Outline each blood parasite and name the species.
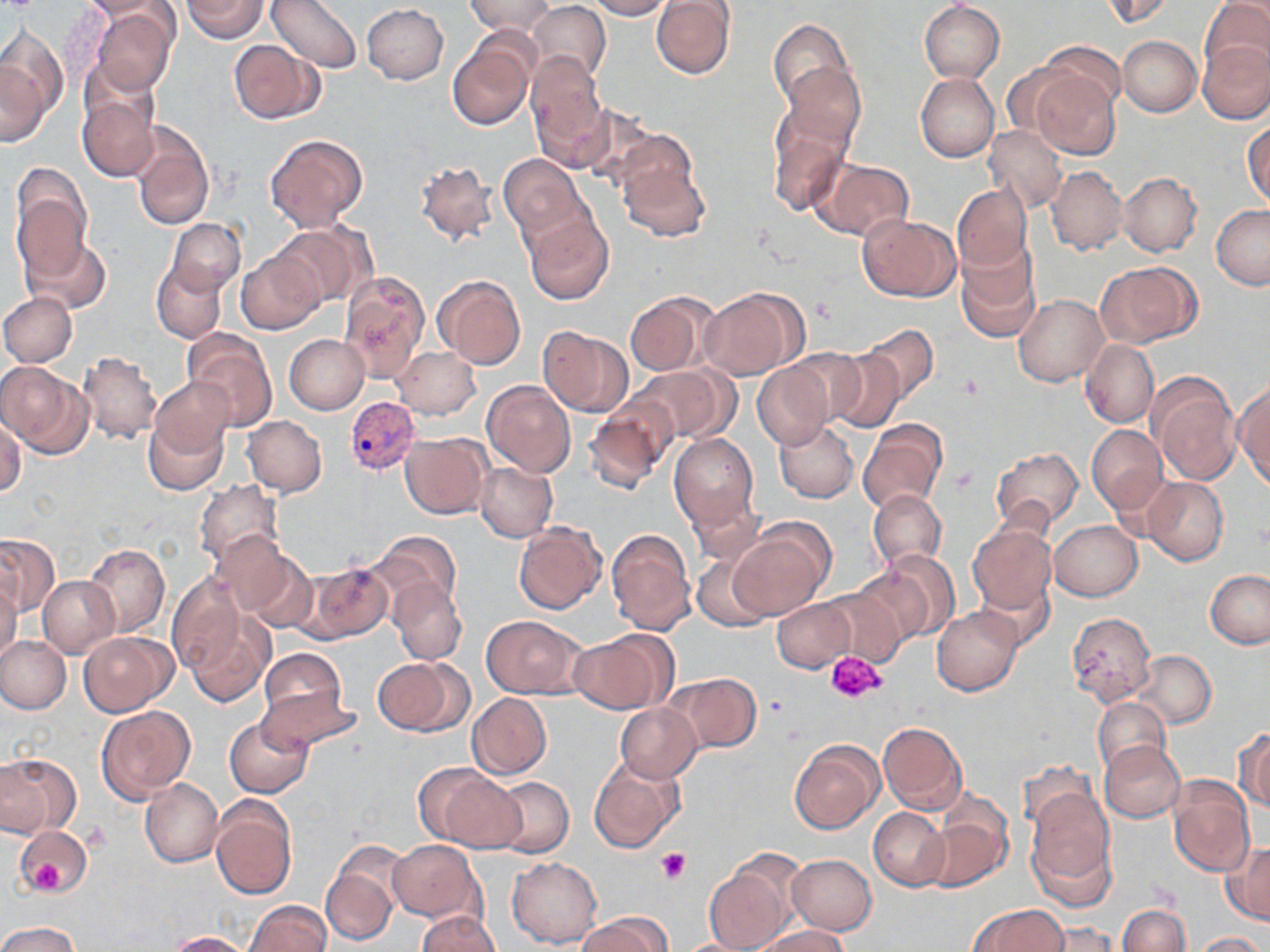
Approximate bounding boxes as (x1, y1, x2, y2) in pixels.
Plasmodium vivax-infected red blood cells: (345, 396, 419, 474).
No Plasmodium falciparum, Plasmodium ovale, Plasmodium malariae, Babesia divergens, or Trypanosoma brucei observed.

slide-level diagnosis = Plasmodium vivax
uninfected red blood cell locations = approximate bounding boxes as (x1, y1, x2, y2) in pixels: (81, 0, 168, 20), (181, 0, 269, 41), (267, 0, 361, 73), (466, 0, 552, 37), (585, 0, 671, 19), (651, 0, 735, 79), (1099, 0, 1174, 26), (1201, 0, 1270, 78), (919, 1, 1005, 82), (527, 2, 611, 84), (361, 4, 448, 84), (90, 6, 177, 95), (769, 19, 852, 109), (0, 25, 70, 124), (1118, 35, 1203, 117), (229, 39, 322, 123), (447, 39, 534, 130), (1199, 40, 1270, 124), (1036, 41, 1125, 123), (526, 53, 609, 165), (1, 56, 51, 146), (782, 63, 866, 149), (1031, 70, 1121, 160), (915, 74, 999, 162), (76, 91, 159, 183), (577, 104, 661, 190), (768, 108, 852, 216), (130, 121, 215, 230), (1243, 121, 1269, 209), (984, 125, 1067, 212), (264, 134, 367, 232), (499, 154, 585, 243), (616, 158, 710, 243), (414, 159, 500, 247), (812, 159, 914, 242), (1045, 166, 1126, 255), (1118, 172, 1202, 257), (952, 183, 1033, 274), (11, 186, 91, 282), (1211, 204, 1270, 289), (523, 212, 613, 305), (858, 214, 959, 301), (166, 218, 245, 295), (272, 222, 372, 307), (24, 235, 111, 315), (958, 243, 1042, 342), (235, 251, 326, 335), (152, 261, 226, 343), (1097, 262, 1200, 348), (338, 271, 429, 383), (435, 275, 526, 370), (701, 289, 803, 380), (0, 292, 76, 366), (626, 292, 713, 377), (1014, 294, 1107, 387), (858, 324, 939, 403), (538, 326, 632, 417), (184, 331, 278, 430), (284, 334, 369, 414), (1081, 339, 1159, 429), (392, 347, 481, 419), (783, 347, 869, 427), (826, 350, 905, 433), (75, 351, 162, 445), (752, 362, 834, 450), (0, 363, 89, 456), (629, 365, 735, 446), (1148, 373, 1241, 485), (151, 376, 234, 460), (1233, 378, 1270, 489), (482, 379, 575, 477), (584, 400, 674, 492), (143, 410, 229, 496), (0, 415, 25, 497), (243, 416, 327, 496), (857, 419, 948, 515), (773, 420, 859, 503), (1086, 425, 1166, 513), (401, 433, 490, 519), (669, 433, 760, 530), (991, 447, 1082, 531), (474, 463, 558, 542), (1142, 477, 1229, 565), (194, 480, 283, 567), (868, 489, 946, 572), (685, 494, 765, 568), (514, 520, 607, 614), (1049, 520, 1142, 600), (729, 522, 832, 619), (967, 524, 1056, 614), (606, 528, 696, 635), (373, 531, 461, 612), (209, 532, 292, 613), (0, 533, 57, 617), (84, 542, 169, 638), (870, 549, 960, 643), (238, 551, 316, 634), (692, 553, 773, 631), (301, 562, 393, 643), (1206, 569, 1270, 650), (165, 575, 244, 677), (974, 575, 1057, 652), (39, 576, 120, 657), (0, 577, 20, 664), (391, 580, 467, 665), (818, 584, 910, 666), (771, 598, 855, 672), (931, 606, 1024, 696), (182, 610, 274, 706), (1066, 612, 1156, 707), (481, 614, 588, 699), (571, 629, 677, 714), (79, 632, 176, 717), (0, 635, 72, 714), (257, 648, 350, 732), (1134, 649, 1216, 728), (372, 657, 468, 737), (668, 672, 761, 754), (256, 684, 362, 752), (467, 692, 553, 780), (1092, 696, 1171, 776), (614, 704, 702, 783), (97, 706, 195, 804), (225, 717, 314, 798), (878, 721, 967, 814), (1235, 728, 1270, 809), (788, 739, 884, 834), (1099, 741, 1185, 823), (0, 753, 80, 838), (589, 756, 686, 854), (423, 766, 521, 855), (1167, 775, 1254, 879), (488, 777, 573, 858), (140, 778, 223, 867), (1025, 788, 1117, 904), (210, 797, 296, 901), (868, 807, 950, 890), (923, 811, 1012, 894), (15, 826, 92, 894), (388, 840, 484, 923), (1223, 843, 1270, 925), (321, 845, 406, 945), (703, 852, 804, 952), (786, 854, 877, 934), (506, 856, 603, 949), (246, 900, 331, 952), (971, 904, 1069, 952), (1117, 905, 1190, 952), (416, 912, 500, 952), (578, 913, 671, 952), (0, 922, 81, 952), (1032, 923, 1120, 951), (753, 925, 851, 952), (166, 931, 255, 952), (1194, 932, 1264, 952)
magnification = 1000x
stain = May-Grünwald-Giemsa
modality = light microscopy
preparation = thin blood smear
platelet locations = approximate bounding boxes as (x1, y1, x2, y2) in pixels: (950, 466, 981, 494), (827, 649, 887, 704), (655, 848, 691, 885), (20, 852, 68, 895)
field of view = one of a larger specimen
image size = 1270×952 pixels